Locate and identify every blood parasite.
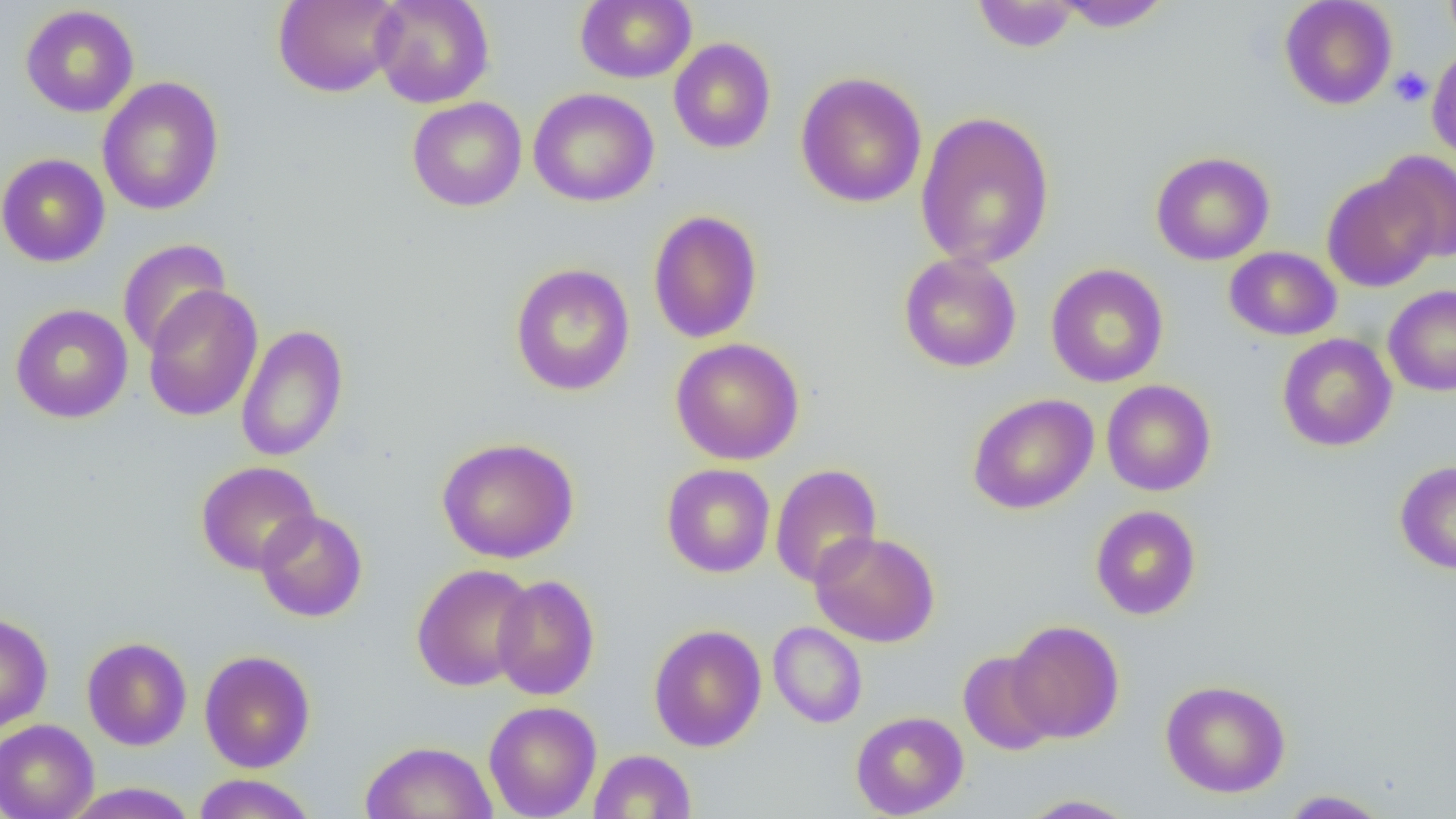

No blood parasites seen.

Summary:
  - Coordinate format: approximate bounding boxes as (x1, y1, x2, y2) in pixels
  - Platelet locations: (1389, 67, 1433, 107)
  - Uninfected red blood cell locations: (273, 0, 404, 98), (371, 0, 495, 108), (575, 0, 697, 84), (1279, 0, 1398, 110), (1442, 0, 1456, 48), (971, 1, 1081, 53), (1053, 1, 1171, 33), (20, 4, 139, 118), (669, 38, 776, 154), (1427, 47, 1456, 162), (795, 71, 927, 209), (97, 77, 225, 216), (528, 87, 659, 207), (407, 97, 527, 211), (915, 111, 1055, 270), (1151, 151, 1274, 265), (1374, 151, 1456, 262), (0, 153, 110, 267), (1322, 171, 1440, 292), (647, 209, 763, 344), (117, 239, 231, 357), (1224, 246, 1341, 341), (898, 253, 1022, 372), (509, 263, 635, 396), (1045, 264, 1169, 388), (142, 285, 263, 422), (1383, 285, 1456, 397), (10, 303, 133, 424), (236, 324, 349, 462), (1277, 333, 1396, 451), (670, 338, 805, 465), (1101, 379, 1216, 496), (967, 393, 1099, 515), (436, 436, 579, 563), (1394, 460, 1456, 574), (195, 461, 321, 575), (661, 463, 775, 578), (770, 464, 883, 589), (1090, 504, 1201, 620), (255, 510, 367, 622), (810, 530, 940, 648), (410, 562, 535, 692), (491, 574, 600, 700), (0, 612, 53, 734), (1007, 620, 1124, 743), (768, 622, 867, 728), (648, 624, 767, 751), (82, 636, 192, 751), (199, 650, 315, 773), (957, 650, 1060, 755), (1160, 679, 1291, 797), (483, 700, 601, 818), (850, 711, 969, 818), (0, 719, 99, 819), (360, 740, 498, 819), (589, 750, 696, 818), (192, 773, 317, 818), (62, 782, 200, 818), (1278, 790, 1391, 818), (1018, 794, 1141, 818)
  - Slide-level diagnosis: negative for blood parasites
  - Magnification: 1000x
  - Field of view: single
  - Preparation: thin blood smear
  - Modality: light microscopy
  - Image size: 1456×819 pixels